Name the blood parasite species.
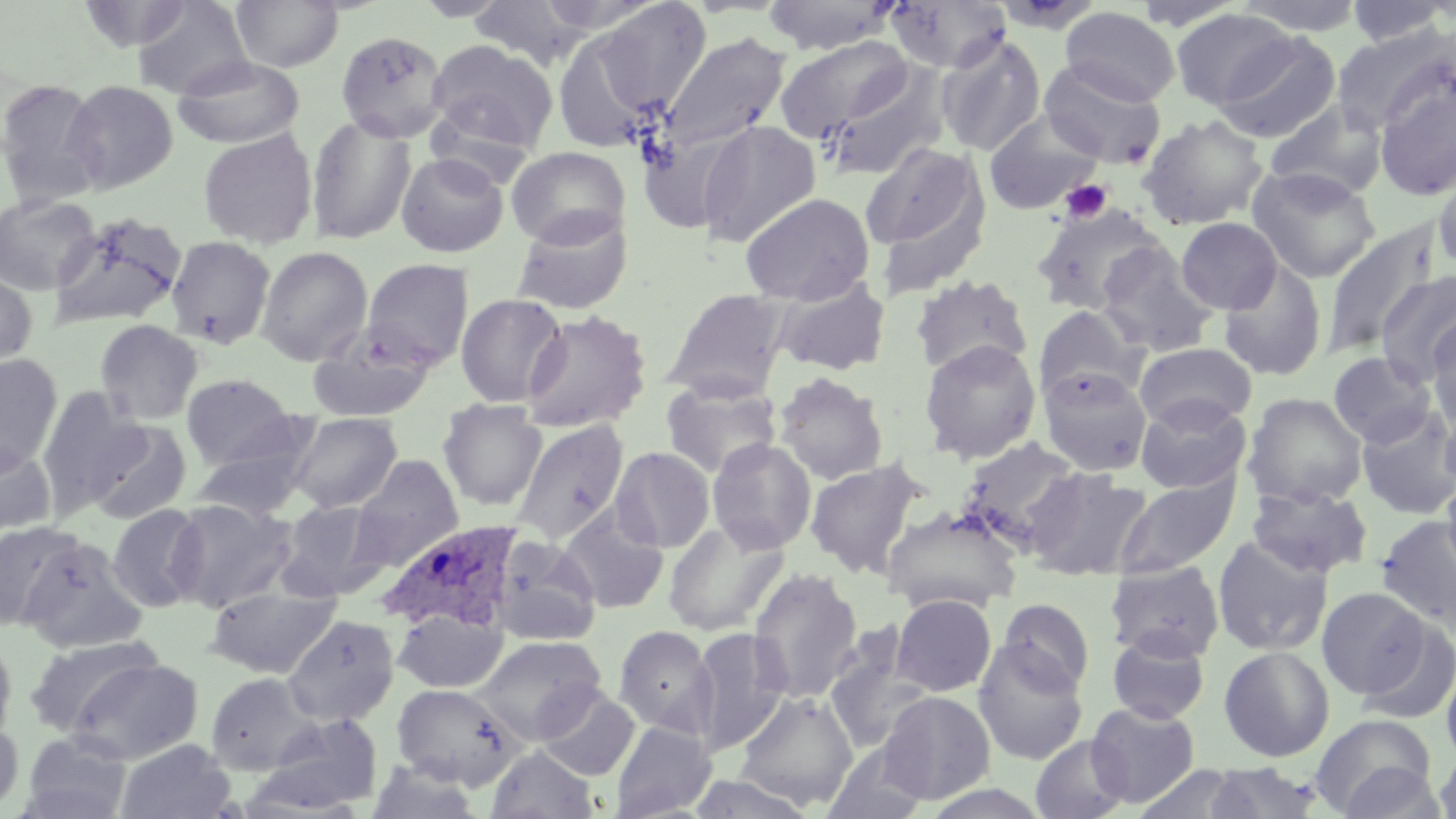

Plasmodium ovale.

Approximate bounding boxes as (x1,y1)-(x2,y2) corner pairs in pixels. Uninfected red blood cell locations: (132,0)-(251,99), (232,0)-(343,71), (579,0)-(712,125), (762,0)-(897,55), (884,0)-(1011,74), (1233,0)-(1369,36), (78,1)-(193,51), (469,1)-(594,68), (1344,1)-(1453,47), (1060,6)-(1180,105), (1170,9)-(1296,110), (550,22)-(671,155), (1331,25)-(1454,134), (335,30)-(449,142), (1213,32)-(1342,144), (656,33)-(791,161), (774,35)-(915,143), (935,35)-(1047,156), (425,40)-(558,157), (173,56)-(305,150), (1038,59)-(1166,169), (819,61)-(951,182), (1372,71)-(1456,200), (0,78)-(105,209), (63,80)-(178,194), (1264,100)-(1389,201), (983,111)-(1105,216), (306,114)-(417,245), (1138,114)-(1268,231), (695,120)-(822,248), (198,128)-(319,249), (859,139)-(990,274), (506,146)-(632,248), (395,152)-(509,257), (1432,162)-(1456,275), (1245,165)-(1381,283), (740,192)-(875,305), (0,193)-(101,295), (1031,203)-(1167,315), (510,209)-(634,315), (49,212)-(187,331), (1175,217)-(1283,314), (1322,220)-(1440,358), (166,235)-(276,348), (1096,242)-(1219,356), (256,246)-(373,366), (361,258)-(475,370), (1219,260)-(1328,382), (0,266)-(38,373), (1376,269)-(1456,385), (909,274)-(1033,376), (772,276)-(891,375), (662,289)-(790,402), (455,293)-(568,408), (1033,305)-(1146,403), (521,309)-(653,433), (1427,312)-(1456,434), (94,319)-(203,424), (308,325)-(436,422), (919,339)-(1041,463), (1133,342)-(1258,430), (1327,352)-(1437,446), (0,354)-(63,472), (1038,367)-(1153,477), (773,372)-(888,485), (181,373)-(296,469), (661,379)-(781,478), (36,388)-(145,513), (1243,392)-(1368,508), (1135,394)-(1252,494), (438,399)-(547,511), (1439,403)-(1456,503), (1355,405)-(1456,520), (287,413)-(403,513), (86,419)-(192,525), (510,419)-(629,545), (190,432)-(318,522), (956,437)-(1083,546), (707,438)-(817,554), (0,443)-(56,538), (610,447)-(715,553), (349,455)-(464,570), (805,458)-(925,578), (1023,467)-(1153,581), (1114,472)-(1240,579), (1441,472)-(1456,584), (1246,483)-(1372,579), (167,498)-(297,612), (277,500)-(387,600), (106,504)-(208,613), (881,506)-(1023,615), (556,507)-(670,615), (1375,515)-(1456,632), (662,520)-(789,637), (0,521)-(79,633), (489,535)-(601,646), (1211,535)-(1333,656), (18,537)-(147,653), (1104,560)-(1225,662), (748,567)-(863,703), (205,585)-(341,678), (1316,587)-(1431,699), (890,594)-(997,696), (996,598)-(1095,693), (393,607)-(507,693), (282,615)-(399,727), (1354,616)-(1456,726), (613,625)-(717,738), (688,629)-(791,754), (1106,630)-(1210,724), (824,633)-(933,754), (24,635)-(161,737), (474,635)-(607,744), (0,637)-(17,746), (972,643)-(1088,764), (1218,645)-(1336,762), (66,657)-(203,764), (1441,661)-(1456,766), (204,672)-(320,775), (391,683)-(524,789), (535,685)-(640,782), (734,691)-(858,810), (879,691)-(995,804), (1086,702)-(1201,807), (255,712)-(384,813), (1310,713)-(1438,817), (0,720)-(23,815), (610,720)-(716,818), (21,731)-(133,819), (1030,734)-(1131,819), (116,739)-(236,819), (822,743)-(931,819), (486,744)-(598,819), (1435,745)-(1456,819), (367,759)-(484,818), (1335,761)-(1448,818), (1202,763)-(1323,818), (1132,765)-(1242,819), (686,772)-(822,817). Plasmodium ovale-infected red blood cell locations: (378,520)-(525,634). Platelet locations: (1061,179)-(1112,223). Captured at 1000x magnification. Thin blood film. Image is 1456×819 pixels. One field of a larger specimen. Light microscopy. May-Grünwald-Giemsa stain.